Classify this cell by malaria status.
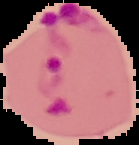
Parasitized.

Summary:
  - Preparation: thin blood smear
  - Image type: cell region segmented out of the field of view; surrounding area masked to black
  - Image size: 139×145 pixels